Describe the morphology of the red blood cells.
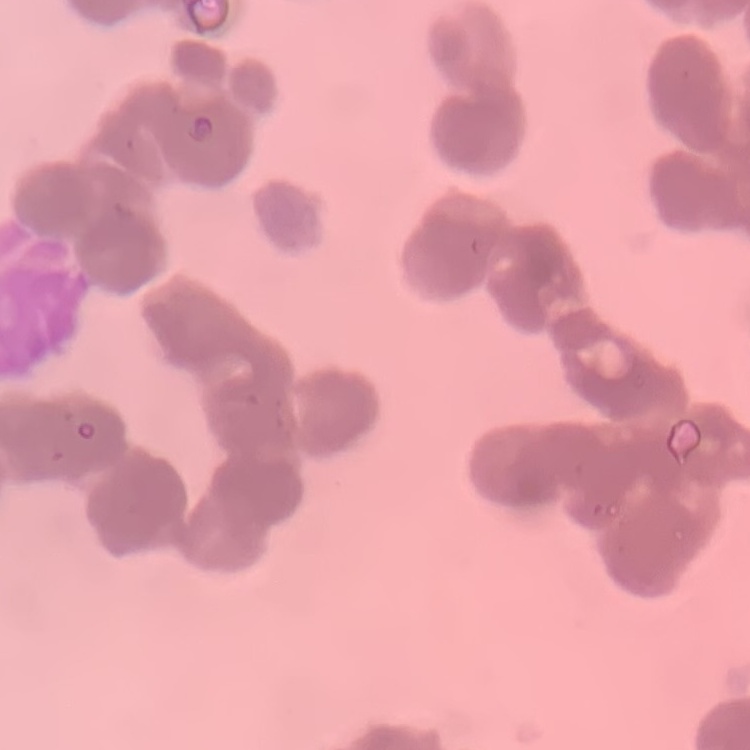

Rouleaux formation.

stain: Field's or Giemsa
preparation: thin blood smear
image_type: square crop of a larger photomicrograph